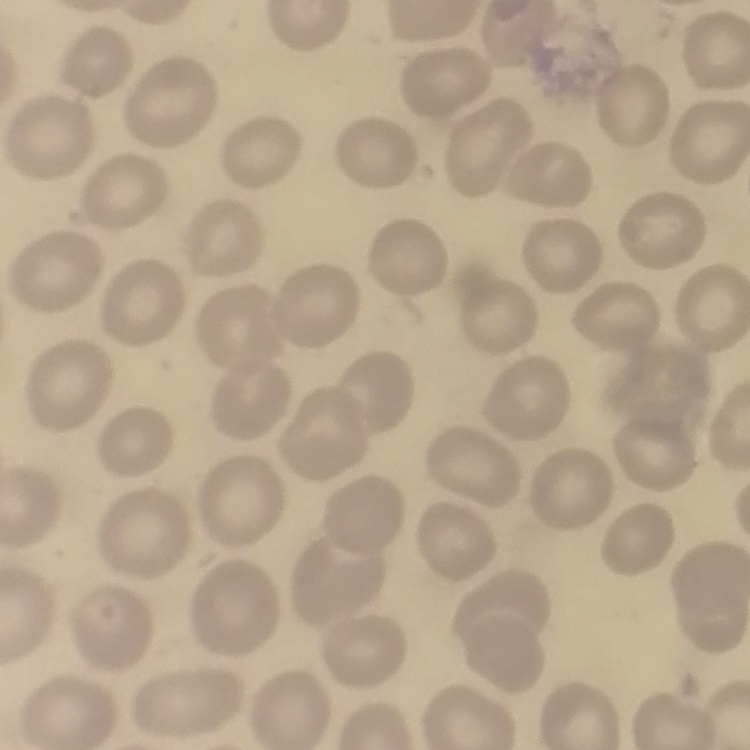

The erythrocytes exhibit no rouleaux formation. Thin blood film. Field's or Giemsa stain. One tile cut from a larger photomicrograph.